Assess the morphology of the erythrocytes.
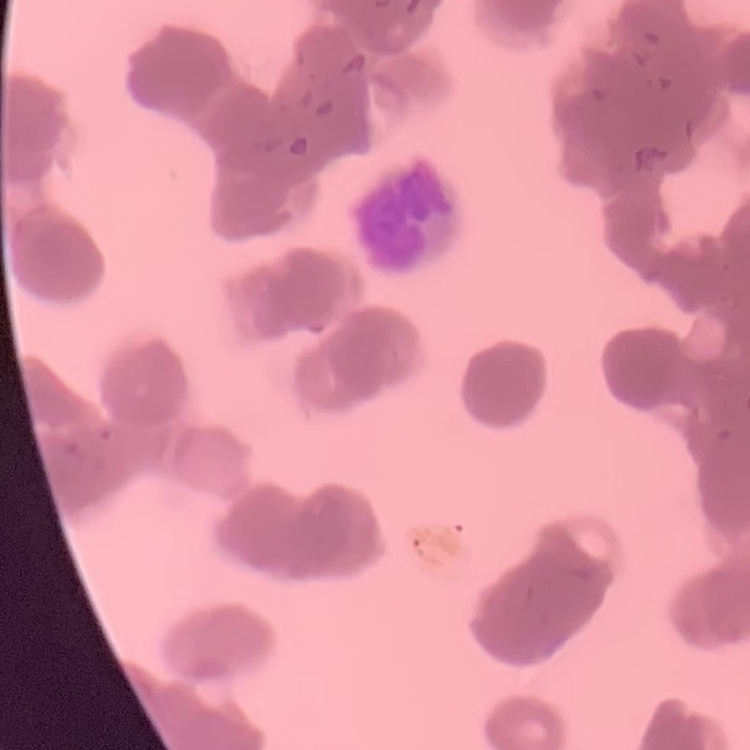
Rouleaux formation.

Summary:
  - Stain: Field's or Giemsa
  - Image type: one tile cut from a larger photomicrograph
  - Preparation: thin peripheral smear